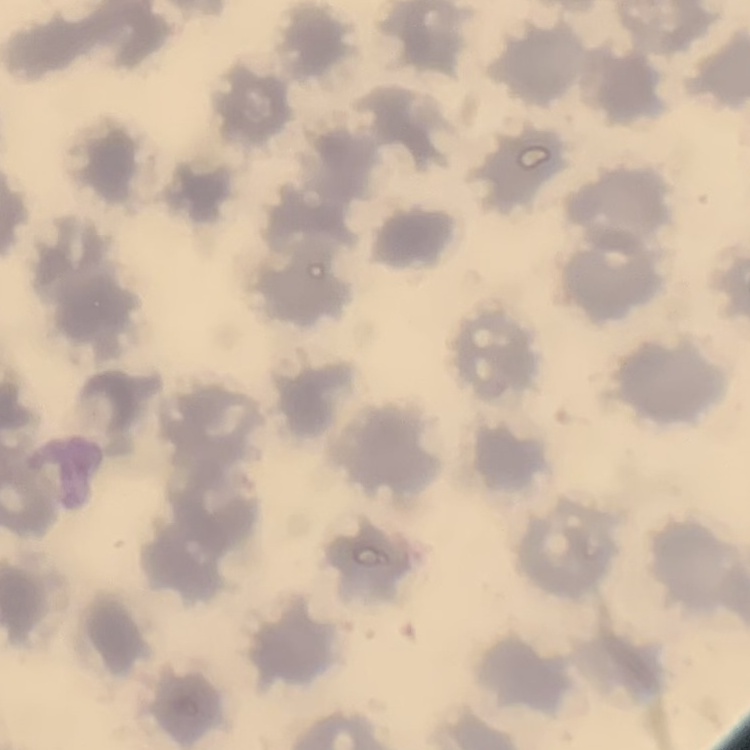
erythrocyte morphology = no rouleaux formation
image type = square crop of a larger photomicrograph
stain = Field's or Giemsa
preparation = thin blood smear